Name the blood parasite species.
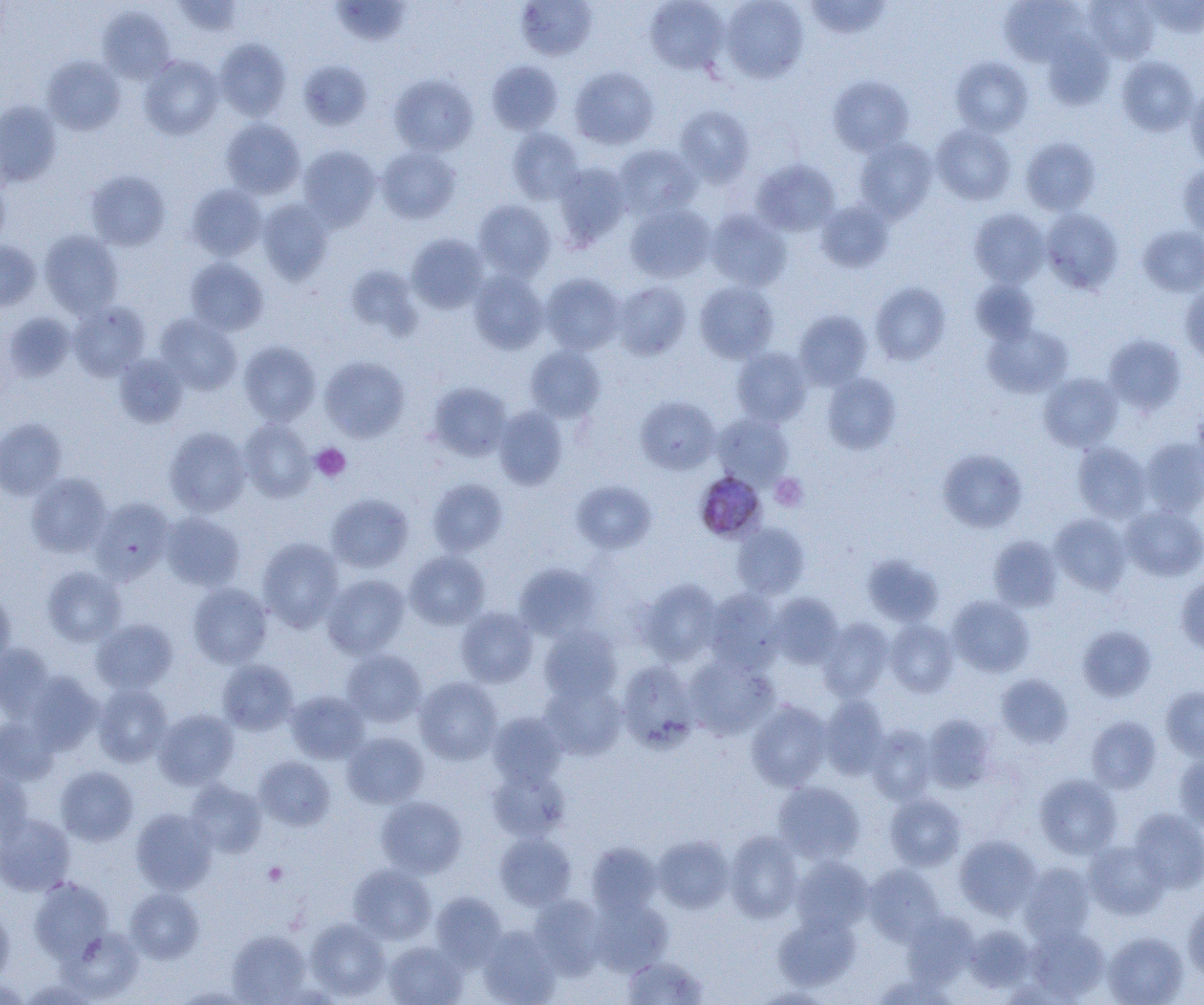
Plasmodium malariae.

Approximate bounding boxes as named x1/y1/x2/y2 corners in pixels. Uninfected red blood cell locations: (x1=173, y1=0, x2=244, y2=37), (x1=516, y1=0, x2=597, y2=61), (x1=645, y1=0, x2=729, y2=74), (x1=721, y1=0, x2=809, y2=83), (x1=1084, y1=0, x2=1160, y2=63), (x1=1143, y1=0, x2=1204, y2=37), (x1=331, y1=1, x2=411, y2=46), (x1=804, y1=1, x2=891, y2=39), (x1=999, y1=1, x2=1083, y2=67), (x1=97, y1=6, x2=176, y2=83), (x1=1043, y1=32, x2=1113, y2=110), (x1=214, y1=38, x2=291, y2=121), (x1=139, y1=55, x2=223, y2=139), (x1=42, y1=56, x2=125, y2=135), (x1=951, y1=56, x2=1033, y2=136), (x1=1116, y1=56, x2=1198, y2=136), (x1=298, y1=59, x2=371, y2=130), (x1=486, y1=61, x2=563, y2=135), (x1=569, y1=66, x2=659, y2=150), (x1=389, y1=74, x2=478, y2=156), (x1=828, y1=75, x2=913, y2=156), (x1=1185, y1=82, x2=1204, y2=169), (x1=0, y1=101, x2=61, y2=187), (x1=675, y1=105, x2=754, y2=186), (x1=221, y1=119, x2=305, y2=199), (x1=931, y1=125, x2=1015, y2=205), (x1=507, y1=127, x2=584, y2=204), (x1=1020, y1=137, x2=1101, y2=215), (x1=854, y1=138, x2=937, y2=222), (x1=298, y1=145, x2=381, y2=230), (x1=614, y1=145, x2=701, y2=219), (x1=377, y1=146, x2=460, y2=223), (x1=752, y1=159, x2=840, y2=236), (x1=554, y1=163, x2=631, y2=246), (x1=1178, y1=165, x2=1204, y2=239), (x1=85, y1=169, x2=171, y2=250), (x1=0, y1=172, x2=11, y2=249), (x1=186, y1=184, x2=267, y2=261), (x1=257, y1=199, x2=334, y2=284), (x1=473, y1=199, x2=556, y2=280), (x1=816, y1=200, x2=894, y2=272), (x1=625, y1=204, x2=715, y2=283), (x1=969, y1=208, x2=1049, y2=287), (x1=1041, y1=209, x2=1123, y2=294), (x1=706, y1=210, x2=791, y2=291), (x1=1138, y1=226, x2=1204, y2=297), (x1=39, y1=230, x2=123, y2=318), (x1=406, y1=233, x2=489, y2=313), (x1=0, y1=240, x2=41, y2=311), (x1=184, y1=257, x2=269, y2=335), (x1=468, y1=269, x2=548, y2=354), (x1=541, y1=273, x2=625, y2=354), (x1=970, y1=280, x2=1040, y2=344), (x1=612, y1=281, x2=691, y2=359), (x1=694, y1=281, x2=778, y2=363), (x1=870, y1=282, x2=951, y2=365), (x1=1179, y1=283, x2=1204, y2=364), (x1=68, y1=302, x2=150, y2=381), (x1=793, y1=310, x2=872, y2=389), (x1=3, y1=312, x2=76, y2=382), (x1=154, y1=314, x2=241, y2=395), (x1=982, y1=323, x2=1074, y2=398), (x1=1103, y1=334, x2=1186, y2=414), (x1=239, y1=340, x2=321, y2=425), (x1=525, y1=345, x2=606, y2=422), (x1=732, y1=347, x2=812, y2=427), (x1=114, y1=354, x2=187, y2=427), (x1=319, y1=355, x2=410, y2=442), (x1=821, y1=372, x2=901, y2=454), (x1=1039, y1=373, x2=1123, y2=451), (x1=427, y1=382, x2=513, y2=461), (x1=635, y1=395, x2=720, y2=474), (x1=494, y1=406, x2=568, y2=490), (x1=1191, y1=410, x2=1204, y2=482), (x1=713, y1=414, x2=793, y2=488), (x1=0, y1=418, x2=66, y2=500), (x1=239, y1=418, x2=316, y2=501), (x1=164, y1=427, x2=251, y2=516), (x1=1140, y1=438, x2=1204, y2=517), (x1=1073, y1=442, x2=1151, y2=522), (x1=938, y1=448, x2=1027, y2=533), (x1=26, y1=472, x2=112, y2=557), (x1=427, y1=479, x2=508, y2=556), (x1=571, y1=480, x2=656, y2=553), (x1=326, y1=493, x2=414, y2=573), (x1=91, y1=499, x2=174, y2=584), (x1=1121, y1=505, x2=1204, y2=581), (x1=161, y1=512, x2=246, y2=590), (x1=1050, y1=514, x2=1131, y2=594), (x1=732, y1=522, x2=809, y2=600), (x1=988, y1=535, x2=1062, y2=612), (x1=257, y1=537, x2=344, y2=632), (x1=405, y1=551, x2=489, y2=629), (x1=862, y1=554, x2=943, y2=627), (x1=514, y1=563, x2=601, y2=640), (x1=42, y1=566, x2=126, y2=647), (x1=1176, y1=572, x2=1204, y2=655), (x1=322, y1=574, x2=410, y2=659), (x1=636, y1=578, x2=723, y2=665), (x1=188, y1=583, x2=272, y2=668), (x1=704, y1=588, x2=784, y2=673), (x1=0, y1=589, x2=16, y2=671), (x1=769, y1=593, x2=843, y2=668), (x1=948, y1=596, x2=1034, y2=677), (x1=456, y1=607, x2=538, y2=687), (x1=818, y1=617, x2=894, y2=700), (x1=91, y1=618, x2=178, y2=694), (x1=885, y1=618, x2=958, y2=697), (x1=539, y1=626, x2=622, y2=705), (x1=1077, y1=626, x2=1156, y2=701), (x1=0, y1=643, x2=56, y2=720), (x1=342, y1=649, x2=426, y2=727), (x1=684, y1=654, x2=779, y2=740), (x1=217, y1=659, x2=299, y2=734), (x1=617, y1=660, x2=699, y2=753), (x1=26, y1=672, x2=103, y2=753), (x1=996, y1=674, x2=1073, y2=747), (x1=414, y1=677, x2=503, y2=764), (x1=541, y1=680, x2=626, y2=760), (x1=92, y1=684, x2=172, y2=767), (x1=1161, y1=686, x2=1204, y2=761), (x1=286, y1=690, x2=369, y2=763), (x1=819, y1=695, x2=889, y2=779), (x1=747, y1=700, x2=832, y2=791), (x1=154, y1=709, x2=238, y2=789), (x1=487, y1=712, x2=568, y2=786), (x1=922, y1=713, x2=997, y2=792), (x1=1086, y1=715, x2=1161, y2=793), (x1=0, y1=716, x2=59, y2=785), (x1=866, y1=724, x2=937, y2=803), (x1=342, y1=731, x2=428, y2=808), (x1=1174, y1=750, x2=1204, y2=831), (x1=254, y1=756, x2=335, y2=830), (x1=55, y1=766, x2=138, y2=845), (x1=487, y1=766, x2=570, y2=841), (x1=0, y1=771, x2=35, y2=848), (x1=1034, y1=774, x2=1121, y2=859), (x1=186, y1=780, x2=267, y2=856), (x1=772, y1=781, x2=866, y2=864), (x1=884, y1=793, x2=966, y2=871), (x1=376, y1=796, x2=467, y2=878), (x1=130, y1=808, x2=217, y2=895), (x1=1130, y1=808, x2=1204, y2=893), (x1=0, y1=813, x2=76, y2=895), (x1=725, y1=830, x2=803, y2=922), (x1=495, y1=832, x2=576, y2=910), (x1=954, y1=834, x2=1041, y2=919), (x1=653, y1=835, x2=734, y2=913), (x1=1084, y1=840, x2=1169, y2=919), (x1=586, y1=842, x2=662, y2=917), (x1=791, y1=856, x2=872, y2=934), (x1=1019, y1=862, x2=1096, y2=944), (x1=348, y1=863, x2=437, y2=944), (x1=863, y1=864, x2=945, y2=946), (x1=29, y1=876, x2=112, y2=962), (x1=125, y1=887, x2=203, y2=963), (x1=430, y1=892, x2=507, y2=968), (x1=529, y1=895, x2=607, y2=978), (x1=589, y1=896, x2=672, y2=975), (x1=1183, y1=900, x2=1204, y2=982), (x1=0, y1=902, x2=14, y2=984), (x1=902, y1=910, x2=979, y2=987), (x1=774, y1=912, x2=861, y2=991), (x1=305, y1=918, x2=391, y2=1001), (x1=477, y1=925, x2=561, y2=1004), (x1=965, y1=925, x2=1036, y2=992), (x1=1025, y1=926, x2=1109, y2=1002), (x1=63, y1=928, x2=143, y2=1001), (x1=227, y1=929, x2=311, y2=1004), (x1=1103, y1=932, x2=1187, y2=1005), (x1=383, y1=941, x2=467, y2=1005), (x1=622, y1=955, x2=708, y2=1004), (x1=0, y1=976, x2=30, y2=1004), (x1=170, y1=985, x2=259, y2=1004), (x1=752, y1=986, x2=837, y2=1004). Platelet locations: (x1=311, y1=444, x2=351, y2=482), (x1=770, y1=473, x2=807, y2=511), (x1=263, y1=861, x2=288, y2=887). Plasmodium malariae-infected red blood cell locations: (x1=694, y1=472, x2=766, y2=543). One field of a larger specimen. Image is 1204×1005 pixels. Captured at 1000x magnification. Thin blood smear. Light microscopy.